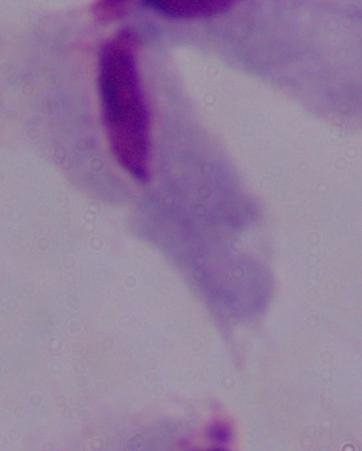
modality = micrograph
identification = trichomonad
magnification = 1000x